State the preparation type.
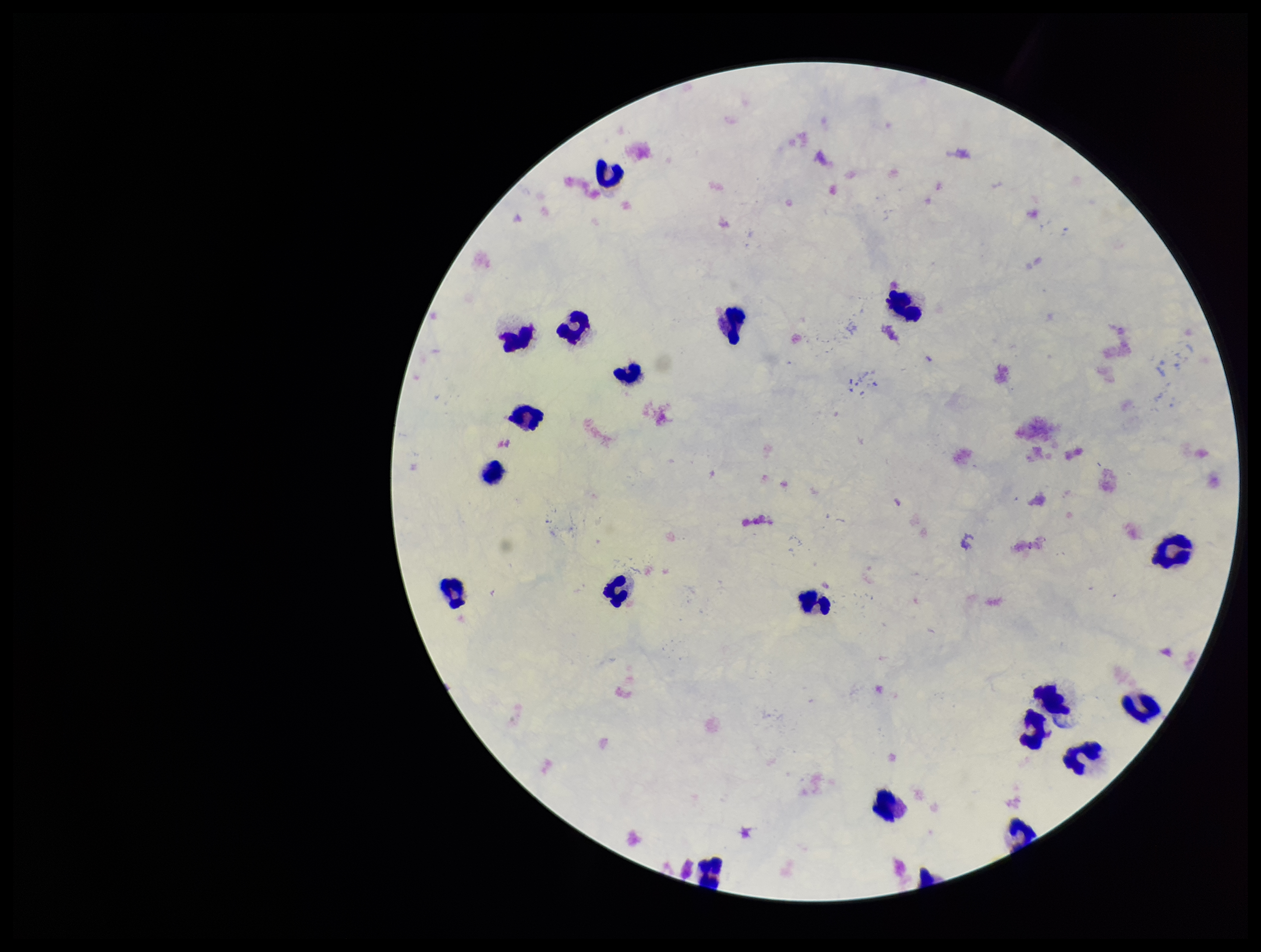

A thick smear.

Smartphone photograph taken through the eyepiece of a microscope. Plasmodium parasites: none detected. Parasite count: 0. Single field of view. Patient malaria status: negative. Image is 1261×952 pixels. Giemsa stain. Leukocyte count: 20.